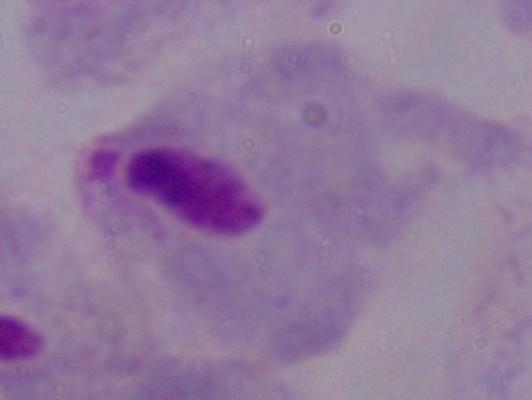
1000x magnification. Micrograph. A trichomonad is seen.